State which parasite is depicted.
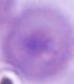

This is Plasmodium.

Micrograph. Captured at either 400x or 1000x magnification.